Give the position of every Plasmodium parasite visible.
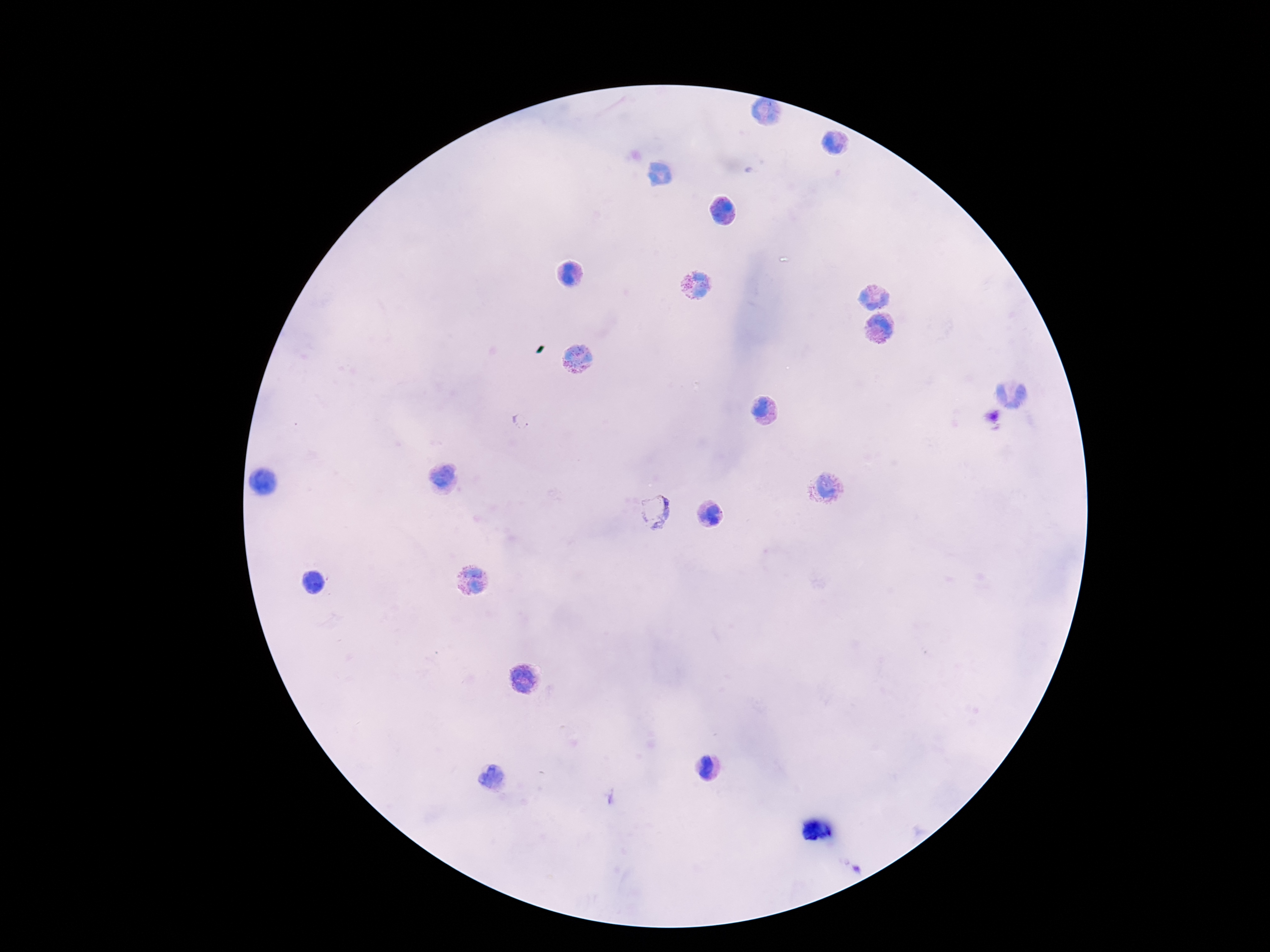
Approximate centers as (x, y) in pixels.
Plasmodium parasites: (522, 421), (655, 511).

{
  "capture": "smartphone camera through the microscope eyepiece",
  "magnification": "100x",
  "image_size": "1270×952 pixels",
  "patient_malaria_status": "infected",
  "preparation": "thick blood smear",
  "field_of_view": "one from this slide",
  "stain": "Giemsa"
}